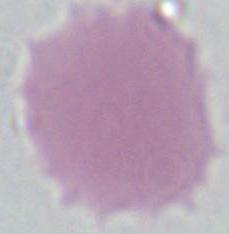 Micrograph. Captured at 1000x magnification. A red blood cell is shown.